Report the malaria status of this cell.
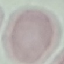
Uninfected.

Giemsa stain. Cell patch, automatically extracted from a larger field of view and resized to 64 × 64 pixels. Thin blood smear. Photographed with a smartphone camera at the microscope eyepiece.